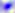
Summary:
  - Magnification: 400x
  - Identification: Toxoplasma gondii
  - Modality: photomicrograph